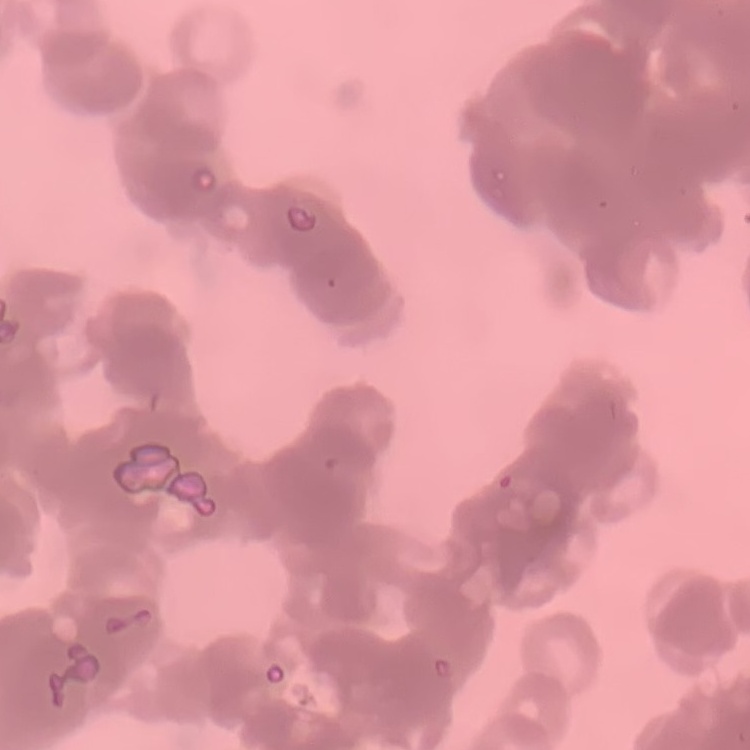
The erythrocytes show rouleaux formation. Stained with either Field's or Giemsa. Square crop of a larger photomicrograph. Thin blood smear.